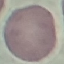
Result: no malaria parasites seen. Automatically extracted cell patch, resized to 64 × 64 pixels. Giemsa-stained preparation. Thin smear of blood. Acquired by smartphone through the microscope eyepiece.